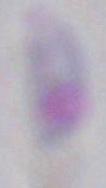

identification = Toxoplasma gondii
magnification = 1000x
modality = micrograph